Classify this cell by malaria status.
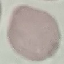
It is uninfected.

Giemsa-stained preparation. Automatically extracted cell patch, resized to 64 × 64 pixels. Thin blood smear. Photographed with a smartphone camera at the microscope eyepiece.